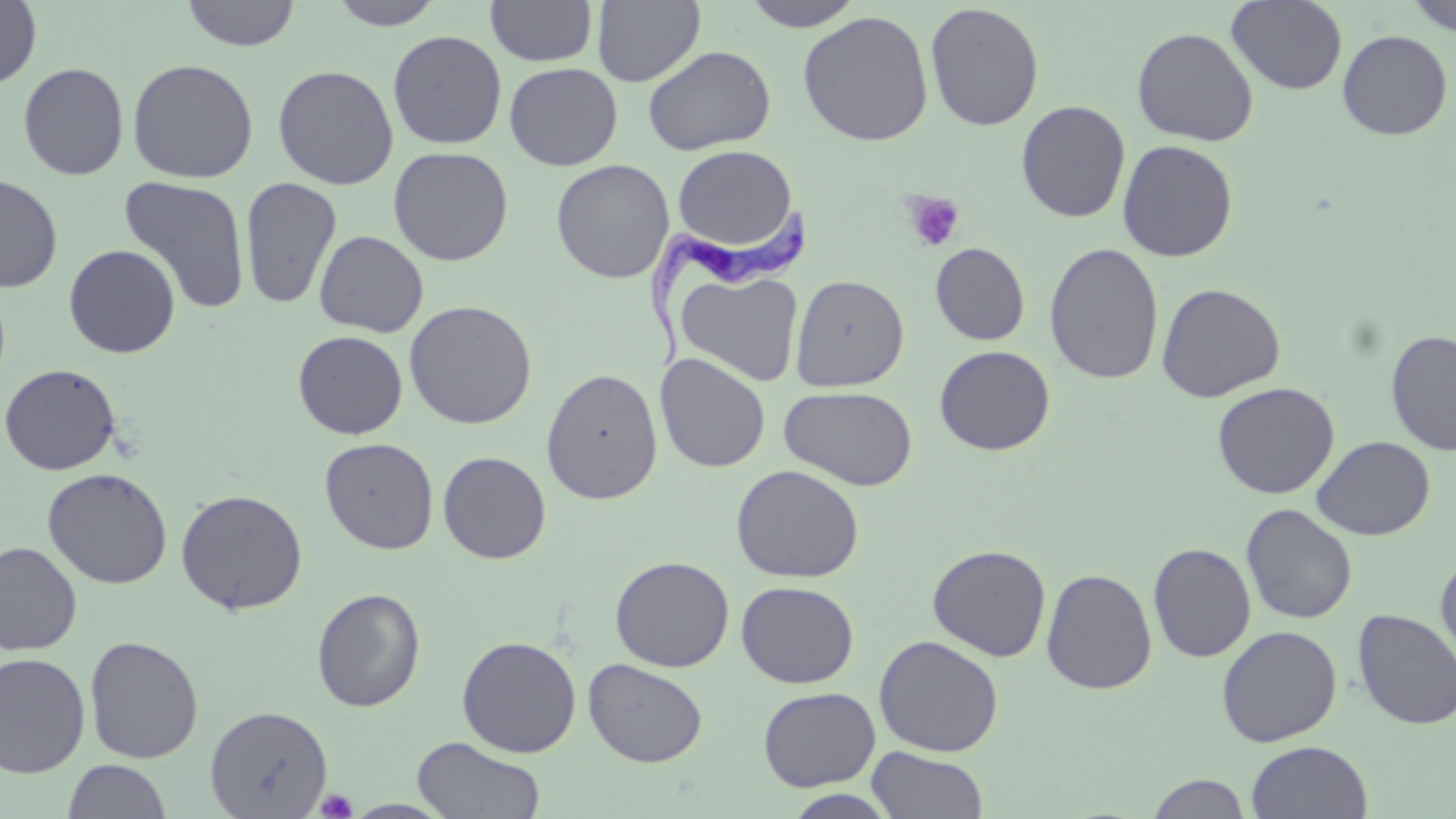

Approximate bounding boxes as [x1, y1, x2, y2] in pixels. Trypanosoma brucei locations: [643, 192, 809, 374]. Platelet locations: [902, 191, 965, 252], [314, 788, 358, 818]. Uninfected red blood cell locations: [181, 0, 301, 51], [327, 0, 445, 29], [485, 0, 598, 67], [740, 0, 864, 31], [1403, 0, 1456, 37], [0, 1, 42, 90], [591, 1, 706, 87], [1226, 1, 1348, 95], [925, 3, 1044, 132], [798, 10, 934, 147], [1132, 26, 1259, 147], [387, 30, 507, 150], [1337, 30, 1453, 141], [642, 45, 776, 156], [127, 58, 259, 183], [17, 62, 129, 180], [504, 62, 623, 170], [272, 64, 399, 190], [1015, 100, 1131, 223], [1117, 139, 1238, 262], [671, 145, 800, 254], [388, 146, 514, 266], [551, 159, 675, 284], [0, 173, 63, 293], [118, 175, 251, 314], [240, 177, 342, 310], [313, 229, 429, 338], [930, 242, 1030, 345], [1044, 242, 1164, 385], [63, 244, 181, 358], [676, 270, 804, 387], [790, 274, 909, 392], [1156, 282, 1286, 402], [404, 300, 537, 429], [1385, 329, 1456, 455], [292, 331, 408, 439], [934, 345, 1055, 456], [655, 353, 771, 473], [0, 363, 121, 475], [541, 367, 663, 505], [1212, 382, 1340, 499], [779, 385, 918, 491], [1311, 436, 1435, 540], [319, 437, 439, 554], [438, 451, 552, 564], [731, 464, 865, 583], [42, 467, 173, 589], [175, 488, 308, 614], [1240, 503, 1358, 625], [0, 541, 82, 655], [1148, 542, 1256, 662], [927, 544, 1052, 662], [1435, 551, 1456, 672], [610, 555, 734, 672], [1041, 567, 1158, 695], [736, 581, 859, 688], [312, 588, 426, 713], [1352, 608, 1456, 731], [1216, 625, 1343, 747], [873, 634, 1004, 757], [84, 635, 204, 763], [456, 635, 581, 757], [0, 652, 91, 778], [583, 658, 708, 768], [758, 686, 880, 791], [204, 704, 333, 817], [412, 737, 546, 818], [1246, 741, 1374, 819], [867, 747, 989, 818], [62, 760, 172, 817], [1145, 773, 1253, 818], [781, 789, 900, 818], [341, 799, 458, 818]. Slide-level diagnosis: Trypanosoma brucei. May-Grünwald-Giemsa stain. Optical microscopy. Thin blood smear. Single field of view. Captured at 1000x magnification. Image is 1456×819 pixels.